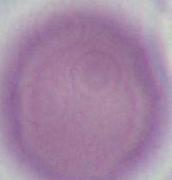
Captured at 1000x magnification. An erythrocyte is shown. Photomicrograph.